Locate and identify every blood parasite.
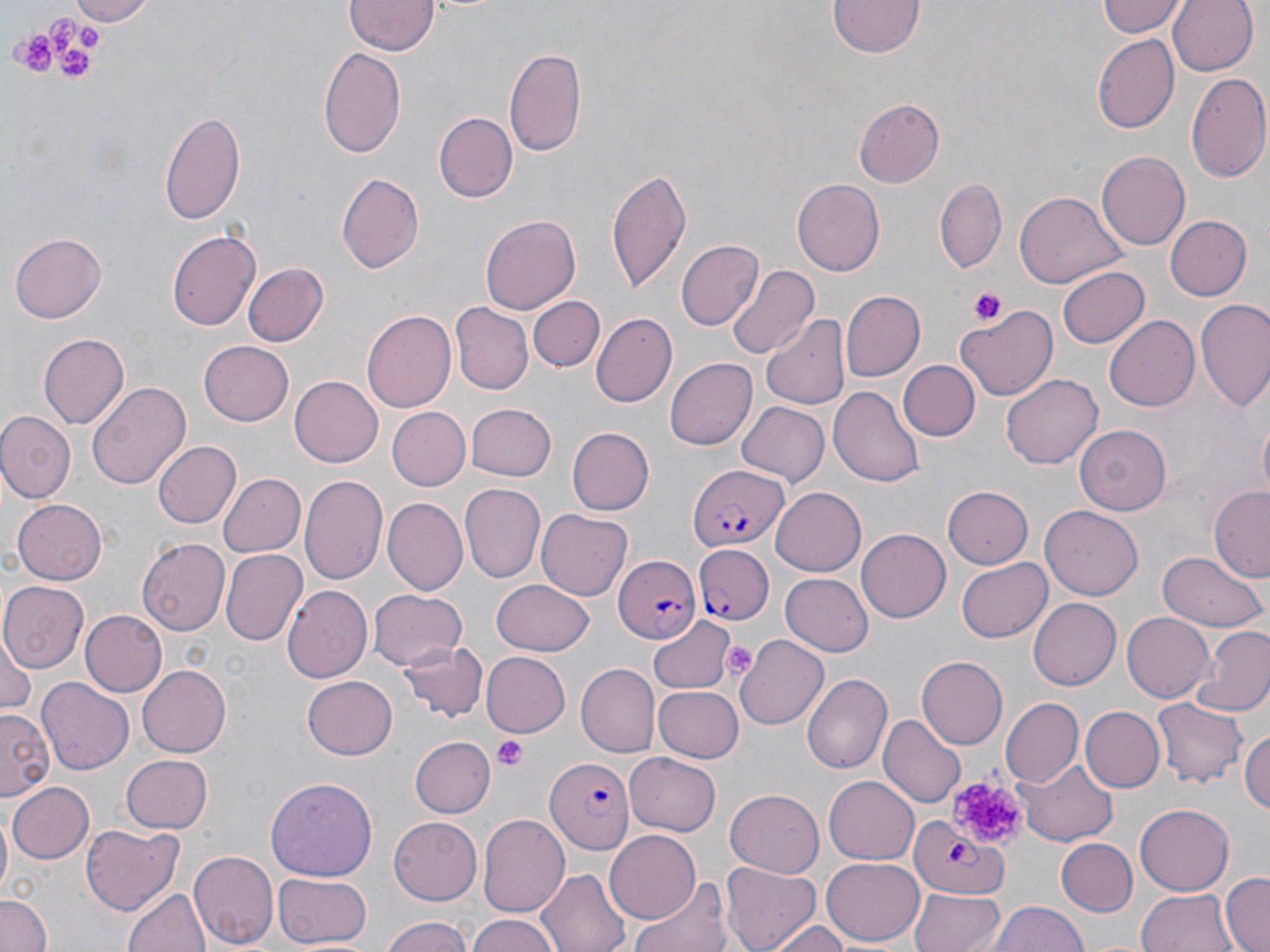

Approximate bounding boxes as (x1, y1, x2, y2) in pixels.
Plasmodium falciparum-infected red blood cells: (687, 465, 788, 553), (691, 538, 772, 628), (615, 556, 700, 643), (548, 760, 635, 853), (910, 817, 1008, 896).
No Plasmodium ovale, Plasmodium malariae, Plasmodium vivax, Babesia divergens, or Trypanosoma brucei observed.

slide-level diagnosis = Plasmodium falciparum
field of view = single
magnification = 1000x
preparation = thin blood film
modality = optical microscopy
stain = May-Grünwald-Giemsa
platelet locations = approximate bounding boxes as (x1, y1, x2, y2) in pixels: (50, 15, 76, 47), (78, 26, 102, 51), (12, 33, 50, 79), (58, 50, 93, 83), (968, 286, 1008, 326), (724, 646, 755, 676), (495, 736, 527, 771), (947, 772, 1024, 845)
image size = 1270×952 pixels
uninfected red blood cell locations = approximate bounding boxes as (x1, y1, x2, y2) in pixels: (61, 0, 153, 23), (1094, 0, 1188, 39), (1168, 0, 1258, 76), (343, 1, 438, 55), (830, 1, 923, 58), (1090, 34, 1179, 134), (319, 44, 406, 161), (505, 47, 586, 157), (1186, 70, 1269, 184), (853, 99, 942, 187), (160, 109, 246, 227), (434, 109, 518, 202), (1097, 152, 1193, 249), (608, 168, 691, 294), (335, 172, 426, 274), (935, 177, 1007, 273), (792, 180, 884, 276), (1017, 191, 1125, 288), (480, 215, 580, 316), (1165, 215, 1252, 300), (167, 229, 261, 333), (10, 232, 106, 322), (676, 239, 763, 331), (243, 263, 329, 347), (726, 263, 818, 361), (1057, 264, 1149, 349), (840, 290, 924, 381), (527, 295, 604, 372), (1194, 299, 1270, 412), (451, 304, 533, 394), (957, 305, 1060, 399), (360, 309, 456, 415), (591, 314, 678, 408), (760, 314, 849, 411), (1103, 316, 1199, 412), (39, 332, 129, 427), (199, 342, 294, 426), (663, 358, 755, 451), (900, 361, 980, 441), (1003, 373, 1102, 470), (290, 374, 385, 466), (88, 381, 189, 493), (831, 384, 926, 488), (737, 402, 828, 487), (465, 403, 555, 482), (388, 407, 469, 490), (0, 412, 74, 502), (1256, 417, 1270, 500), (1077, 424, 1169, 515), (565, 427, 653, 516), (152, 441, 241, 529), (217, 472, 305, 558), (299, 476, 387, 588), (458, 484, 545, 585), (942, 486, 1033, 569), (1210, 487, 1270, 581), (770, 488, 865, 575), (382, 497, 467, 595), (13, 499, 107, 583), (1041, 506, 1144, 598), (536, 510, 633, 599), (857, 527, 952, 623), (137, 539, 228, 636), (1157, 549, 1266, 631), (219, 550, 306, 647), (957, 557, 1052, 643), (780, 574, 873, 656), (489, 579, 596, 656), (1, 581, 88, 672), (282, 584, 371, 684), (369, 589, 466, 673), (1027, 598, 1121, 690), (81, 610, 166, 696), (1122, 612, 1214, 701), (647, 613, 735, 692), (1191, 627, 1270, 717), (0, 635, 37, 717), (735, 636, 830, 728), (400, 641, 488, 721), (480, 652, 569, 737), (918, 656, 1007, 747), (576, 663, 659, 757), (136, 664, 230, 758), (804, 674, 891, 775), (301, 677, 398, 760), (38, 678, 134, 774), (654, 684, 745, 760), (999, 698, 1083, 788), (1153, 699, 1245, 787), (1080, 707, 1163, 792), (1, 712, 53, 798), (880, 714, 966, 810), (1241, 728, 1270, 817), (409, 737, 493, 818), (625, 751, 722, 835), (120, 753, 213, 832), (1021, 759, 1117, 845), (823, 775, 920, 864), (266, 776, 379, 881), (9, 781, 93, 864), (726, 788, 824, 877), (1137, 804, 1233, 895), (0, 810, 12, 899), (478, 814, 570, 918), (389, 818, 482, 903), (80, 822, 183, 918), (607, 830, 702, 923), (1058, 838, 1137, 916), (187, 849, 277, 950), (822, 858, 924, 945), (720, 861, 822, 952), (539, 868, 631, 952), (270, 873, 373, 950), (1220, 873, 1269, 952), (634, 876, 735, 952), (123, 885, 210, 952), (911, 888, 1006, 952), (1136, 889, 1237, 952), (0, 894, 52, 952), (987, 899, 1088, 952), (465, 913, 565, 952), (379, 914, 473, 952), (768, 921, 853, 951)